Locate every malaria parasite and every leukocyte.
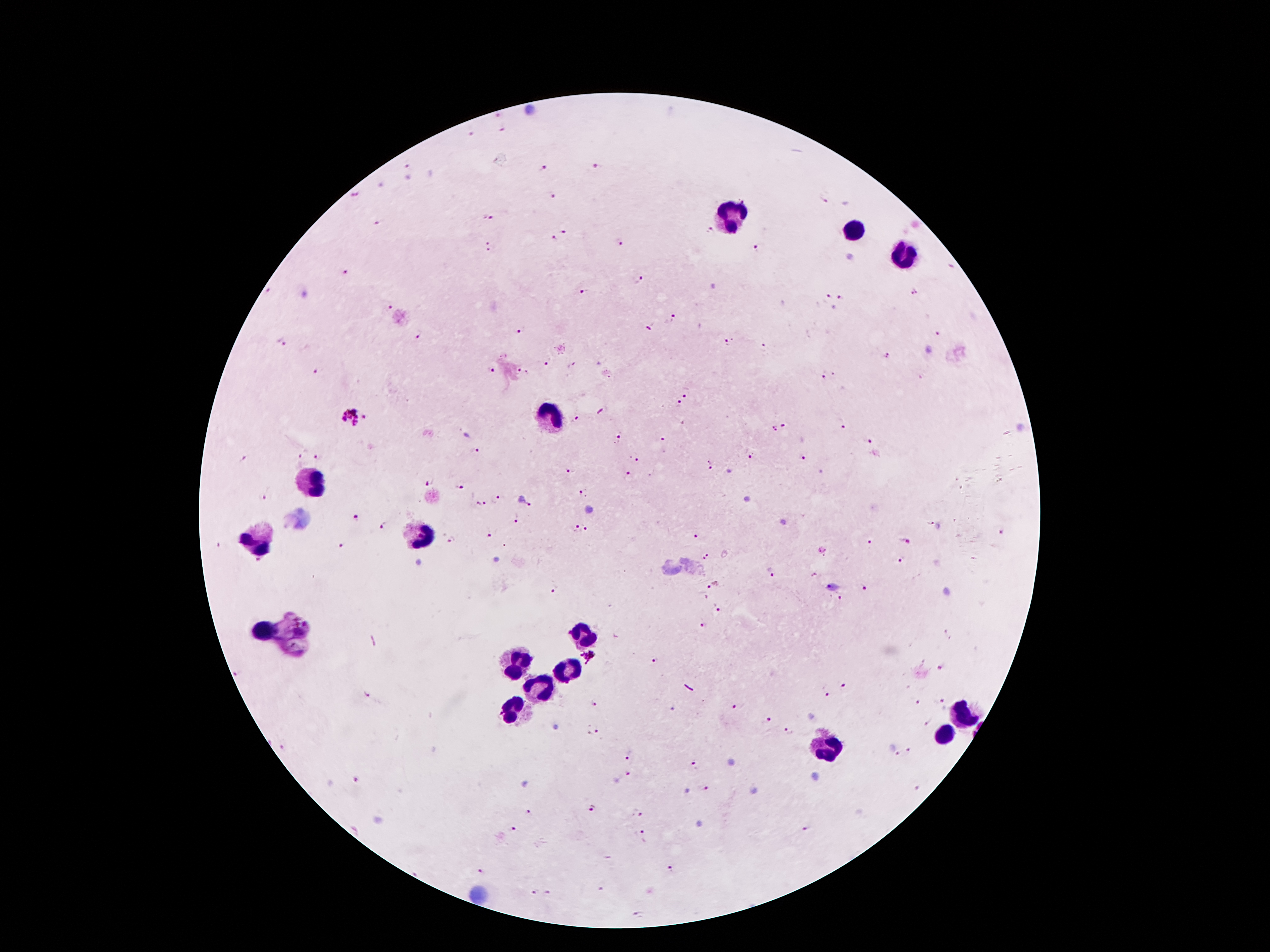
Approximate centers as (x, y) in pixels.
Malaria parasites: (495, 118), (503, 129), (471, 134), (408, 166), (596, 167), (544, 169), (353, 195), (551, 197), (824, 199), (489, 216), (379, 221), (709, 230), (565, 232), (554, 240), (621, 241), (491, 247), (755, 248), (345, 275), (638, 279), (583, 292), (914, 294), (829, 297), (842, 300), (388, 306), (672, 317), (649, 327), (521, 330), (417, 335), (939, 336), (283, 343), (727, 343), (762, 344), (888, 357), (548, 360), (494, 370), (314, 372), (523, 373), (823, 376), (684, 395), (679, 404), (349, 416), (365, 416), (575, 419), (839, 424), (784, 426), (774, 429), (617, 438), (662, 440), (869, 442), (474, 451), (298, 456), (316, 456), (636, 457), (751, 457), (802, 458), (244, 459), (708, 466), (568, 472), (628, 475), (429, 482), (458, 487), (583, 493), (496, 497), (262, 498), (479, 504), (531, 505), (517, 517), (357, 518), (383, 524), (588, 528), (576, 530), (1003, 534), (488, 535), (693, 537), (450, 541), (869, 541), (905, 541), (340, 545), (707, 556), (901, 561), (257, 563), (771, 573), (712, 587), (555, 590), (864, 591), (840, 599), (718, 609), (704, 625), (948, 634), (588, 658), (655, 660), (943, 667), (844, 685), (369, 695), (824, 695), (942, 701), (593, 703), (919, 703), (733, 706), (768, 720), (927, 726), (596, 732), (788, 732), (909, 748), (897, 754), (629, 757), (696, 766), (626, 776), (356, 780), (706, 788), (917, 790), (593, 809), (528, 812), (635, 814), (513, 830), (807, 830), (641, 832), (667, 870), (482, 872), (598, 889), (532, 891), (544, 891), (637, 915).
Leukocytes: (731, 218), (853, 230), (904, 256), (548, 413), (310, 484), (422, 535), (254, 542), (263, 631), (580, 634), (515, 664), (568, 669), (538, 690), (511, 714), (959, 715), (943, 736), (827, 746).

Summary:
  - Image size: 1270×952 pixels
  - Stain: Giemsa
  - Field of view: one from this slide
  - Capture: smartphone through the microscope eyepiece
  - Magnification: 100x
  - Preparation: thick blood film
  - Patient malaria status: infected with Plasmodium falciparum